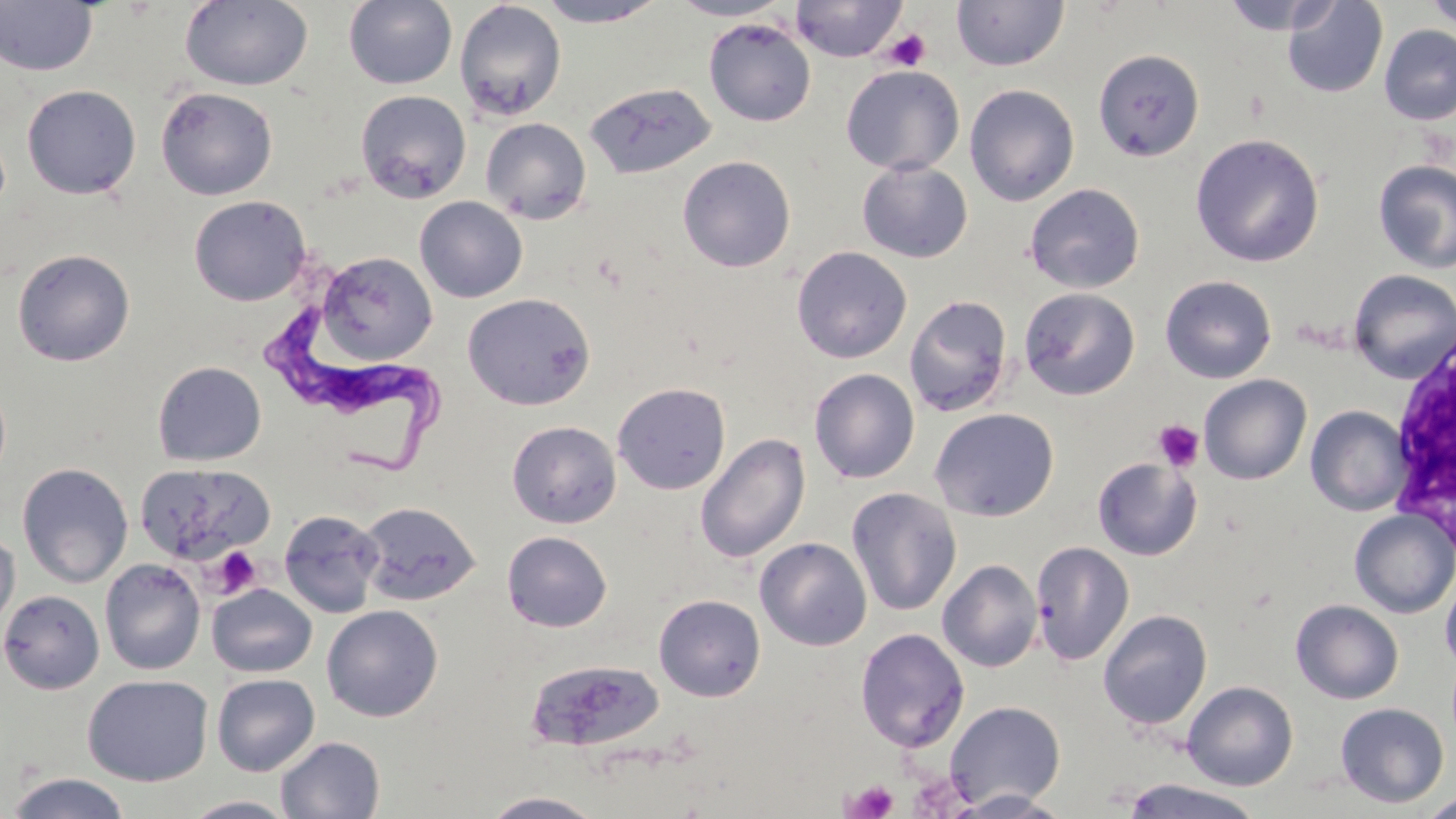

Approximate bounding boxes as [x1, y1, x2, y2] in pixels. White blood cell locations: [1386, 323, 1456, 546]. Uninfected red blood cell locations: [180, 0, 313, 90], [343, 0, 458, 90], [533, 0, 670, 27], [668, 0, 791, 20], [790, 0, 907, 62], [950, 0, 1069, 72], [1222, 0, 1338, 35], [1282, 0, 1387, 99], [1424, 0, 1455, 31], [0, 1, 98, 77], [454, 1, 566, 122], [704, 18, 816, 127], [1379, 24, 1456, 125], [1092, 48, 1204, 162], [840, 65, 965, 176], [584, 81, 717, 180], [21, 84, 141, 199], [964, 84, 1080, 207], [155, 86, 278, 200], [355, 90, 471, 203], [480, 118, 592, 224], [1190, 133, 1325, 267], [677, 155, 796, 273], [1374, 159, 1456, 273], [857, 160, 973, 263], [1025, 184, 1145, 293], [189, 195, 311, 306], [414, 196, 528, 303], [791, 245, 912, 363], [12, 248, 135, 366], [317, 251, 436, 365], [1348, 269, 1456, 382], [1159, 275, 1277, 383], [1019, 287, 1140, 400], [462, 292, 596, 411], [904, 295, 1013, 417], [153, 361, 266, 466], [809, 368, 920, 484], [1199, 374, 1311, 485], [612, 382, 731, 495], [1306, 405, 1411, 516], [929, 408, 1060, 522], [506, 420, 621, 528], [695, 433, 811, 563], [1092, 457, 1201, 560], [17, 462, 133, 588], [134, 462, 275, 567], [845, 487, 962, 616], [358, 501, 481, 607], [279, 509, 385, 618], [1349, 509, 1456, 618], [0, 530, 20, 631], [502, 531, 612, 632], [755, 537, 872, 651], [1030, 542, 1134, 666], [99, 558, 206, 675], [938, 559, 1043, 672], [1440, 571, 1456, 673], [207, 582, 317, 678], [0, 588, 104, 694], [654, 594, 766, 701], [1290, 599, 1404, 704], [321, 605, 443, 722], [1097, 609, 1212, 730], [855, 628, 970, 752], [525, 659, 666, 753], [212, 673, 320, 776], [82, 674, 213, 786], [1182, 681, 1298, 790], [944, 700, 1066, 809], [1334, 702, 1450, 808], [275, 735, 385, 818], [4, 772, 133, 819], [1123, 779, 1263, 818], [947, 790, 1074, 818], [480, 791, 606, 818], [1418, 792, 1456, 818], [182, 796, 300, 819]. Platelet locations: [883, 28, 931, 71], [1153, 420, 1204, 471], [210, 545, 264, 597], [845, 780, 899, 818]. Trypanosoma brucei locations: [263, 305, 454, 473]. Slide-level diagnosis: Trypanosoma brucei. May-Grünwald-Giemsa-stained preparation. Image is 1456×819 pixels. 1000x magnification. One field of a larger specimen. Thin blood smear. Optical microscopy.